Assess this cell for malaria.
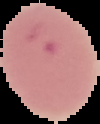

It is parasitized.

Summary:
  - Preparation: thin blood film
  - Image size: 100×124 pixels
  - Image type: cell region segmented out of the field of view; surrounding area masked to black